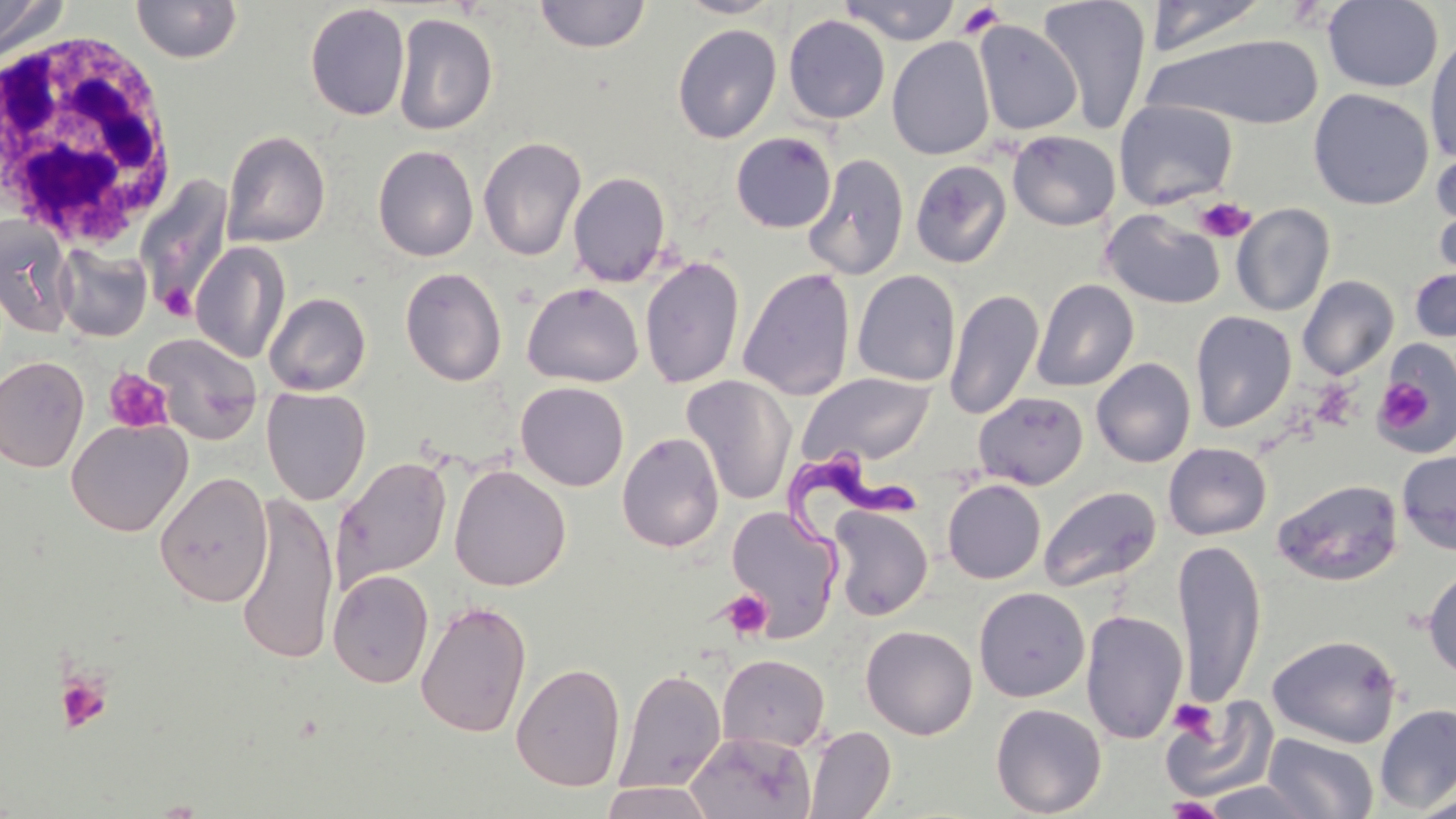

Summary:
  - Coordinate format: approximate bounding boxes as [x1, y1, x2, y2] in pixels
  - Trypanosoma brucei locations: [780, 451, 921, 617]
  - White blood cell locations: [4, 23, 184, 250]
  - Uninfected red blood cell locations: [0, 0, 66, 61], [130, 0, 244, 64], [534, 0, 652, 54], [675, 0, 786, 19], [839, 0, 961, 45], [1037, 0, 1153, 134], [1144, 0, 1271, 57], [1322, 0, 1444, 92], [305, 3, 410, 121], [392, 13, 498, 135], [783, 15, 890, 124], [973, 20, 1082, 136], [673, 23, 782, 144], [1424, 31, 1456, 166], [1148, 33, 1326, 130], [887, 37, 996, 160], [1308, 88, 1434, 210], [1114, 99, 1238, 211], [1006, 119, 1236, 225], [222, 129, 331, 248], [1007, 130, 1121, 231], [731, 132, 837, 233], [477, 136, 587, 262], [372, 144, 479, 262], [1430, 146, 1456, 273], [802, 153, 909, 280], [910, 160, 1012, 269], [568, 171, 671, 287], [135, 175, 236, 319], [1231, 203, 1335, 317], [1101, 207, 1226, 310], [0, 217, 75, 336], [190, 241, 290, 364], [54, 243, 152, 342], [639, 256, 744, 389], [1409, 264, 1456, 344], [400, 266, 507, 386], [738, 267, 855, 400], [852, 270, 961, 387], [1297, 275, 1399, 380], [1031, 278, 1139, 392], [522, 281, 644, 387], [944, 288, 1044, 421], [264, 291, 371, 396], [1190, 311, 1297, 433], [144, 333, 263, 444], [1374, 339, 1456, 456], [0, 355, 89, 473], [1092, 358, 1196, 468], [799, 372, 936, 469], [681, 376, 797, 506], [515, 381, 629, 491], [261, 388, 371, 505], [974, 391, 1088, 490], [66, 418, 192, 536], [616, 431, 724, 553], [1163, 442, 1272, 540], [1396, 449, 1456, 556], [332, 455, 452, 589], [449, 464, 571, 591], [153, 471, 273, 607], [942, 479, 1046, 584], [1272, 479, 1404, 586], [1038, 485, 1161, 593], [234, 493, 340, 666], [726, 505, 842, 642], [828, 505, 933, 621], [1173, 538, 1266, 710], [1422, 565, 1456, 683], [328, 569, 434, 689], [974, 587, 1090, 702], [414, 599, 532, 739], [1080, 609, 1188, 745], [861, 625, 978, 740], [1266, 633, 1403, 749], [717, 653, 831, 754], [511, 661, 626, 791], [615, 667, 726, 793], [1161, 698, 1278, 801], [990, 702, 1107, 817], [1375, 704, 1456, 812], [804, 725, 896, 818], [684, 730, 816, 819], [1262, 732, 1379, 818], [1199, 779, 1324, 818], [598, 782, 716, 818], [1409, 791, 1456, 819]
  - Platelet locations: [957, 3, 1005, 38], [1196, 197, 1255, 243], [161, 285, 194, 321], [103, 368, 174, 434], [1382, 381, 1430, 430], [721, 589, 772, 640], [54, 670, 113, 732], [1168, 698, 1219, 740], [1162, 796, 1227, 819]
  - Slide-level diagnosis: Trypanosoma brucei
  - Magnification: 1000x
  - Preparation: thin blood film
  - Field of view: one of a larger specimen
  - Image size: 1456×819 pixels
  - Stain: May-Grünwald-Giemsa
  - Modality: optical microscopy